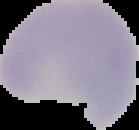 Result: no malaria parasites detected. From a thin blood smear. Cell region segmented out of the field of view; the surrounding area is masked to black. Image is 139×130 pixels.